Classify this cell by malaria status.
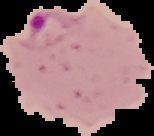

It is parasitized.

image size = 154×136 pixels
preparation = thin blood smear
image type = cell region segmented out of the field of view; surrounding area masked to black